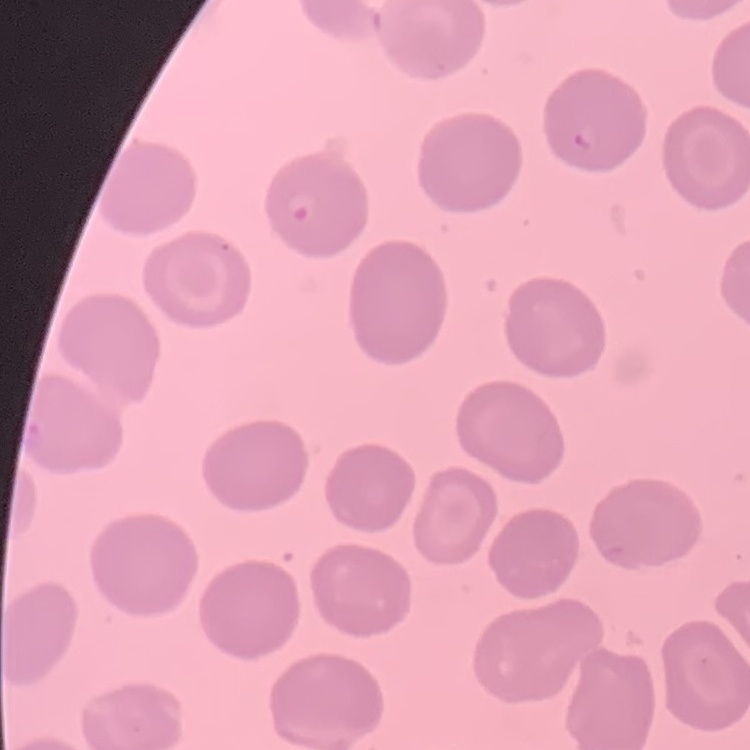

Summary:
  - Red blood cell morphology: no rouleaux formation
  - Image type: one tile cut from a larger photomicrograph
  - Preparation: thin blood smear
  - Stain: Field's or Giemsa